Classify this cell by malaria status.
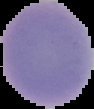
Uninfected.

preparation: thin blood film
image_size: 94×109 pixels
image_type: segmented cell region on a black background